Identify the blood parasite species.
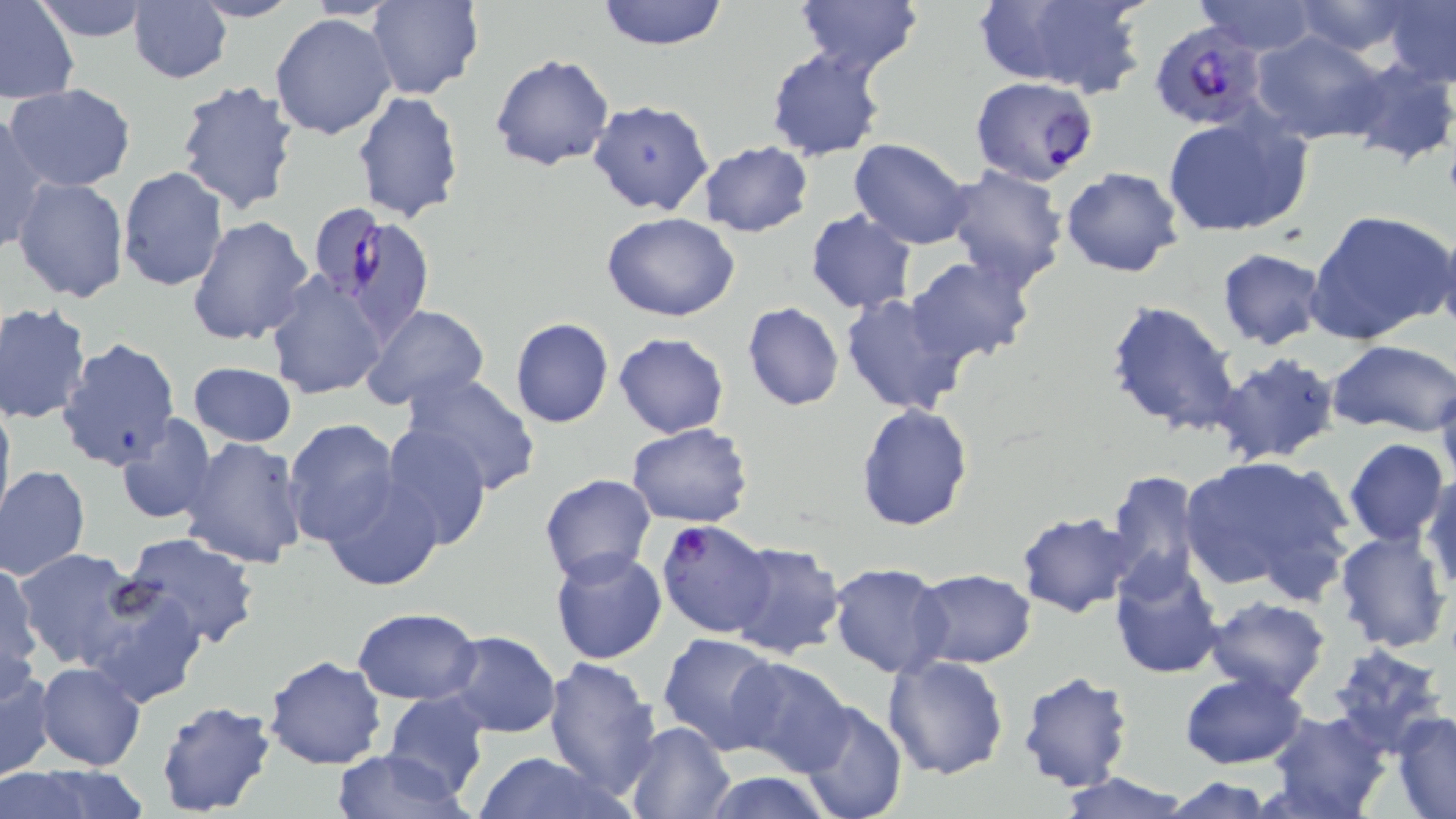

Plasmodium falciparum.

image size = 1456×819 pixels
uninfected red blood cell locations (subset) = approximate bounding boxes as (x1, y1, x2, y2) in pixels: (0, 0, 80, 104), (30, 0, 154, 42), (128, 0, 232, 85), (596, 0, 729, 50), (980, 0, 1147, 97), (1193, 0, 1322, 53), (189, 1, 302, 23), (366, 1, 483, 100), (795, 1, 923, 79), (1289, 1, 1419, 58), (1383, 1, 1455, 88), (269, 12, 399, 141), (1252, 31, 1389, 145), (766, 46, 889, 162), (489, 53, 615, 172), (1339, 57, 1456, 168), (175, 78, 302, 216), (5, 83, 137, 193), (352, 91, 465, 225), (587, 101, 715, 218), (1, 112, 51, 258), (1162, 112, 1312, 238), (847, 136, 976, 250), (698, 141, 813, 236), (941, 164, 1069, 292), (117, 166, 230, 293), (1060, 166, 1181, 278), (12, 176, 128, 304), (1307, 209, 1456, 346), (804, 210, 917, 314), (603, 212, 740, 323), (187, 215, 315, 345), (1435, 227, 1456, 336), (1216, 247, 1327, 349), (908, 256, 1033, 364), (264, 273, 388, 399), (839, 291, 968, 416), (1103, 299, 1241, 437), (0, 302, 94, 425), (742, 302, 844, 412), (361, 305, 491, 412), (509, 317, 614, 428), (612, 333, 730, 438), (61, 338, 179, 472), (1328, 340, 1456, 435), (1212, 351, 1341, 466), (187, 362, 298, 447), (401, 372, 543, 497), (1434, 379, 1456, 494), (0, 393, 15, 529), (855, 404, 972, 532), (113, 413, 218, 526), (283, 418, 402, 547), (625, 423, 753, 528), (377, 425, 491, 551), (1343, 437, 1450, 546), (180, 438, 310, 570), (1178, 455, 1353, 597), (0, 464, 91, 581), (1104, 469, 1205, 592), (321, 470, 442, 591), (1423, 471, 1456, 595), (539, 474, 657, 586), (1015, 510, 1137, 618), (1334, 527, 1452, 653), (119, 532, 262, 652), (725, 540, 847, 659), (13, 547, 147, 672), (550, 547, 669, 664), (1109, 555, 1225, 677), (0, 559, 41, 693), (828, 563, 951, 678), (908, 568, 1036, 669), (76, 579, 207, 709), (1203, 596, 1332, 702), (353, 607, 482, 705), (444, 631, 562, 737), (658, 634, 782, 754), (1326, 643, 1449, 754), (263, 656, 385, 771), (544, 656, 663, 801), (882, 656, 1010, 780), (726, 658, 853, 776), (35, 662, 146, 772), (0, 664, 56, 780), (1016, 669, 1136, 791), (1178, 672, 1308, 769), (383, 690, 490, 799), (153, 699, 276, 817), (794, 699, 907, 819), (1267, 710, 1392, 819), (1391, 711, 1456, 817), (624, 721, 733, 819), (332, 749, 470, 818), (472, 751, 626, 819), (24, 764, 149, 819), (2, 769, 85, 818), (1052, 771, 1193, 818), (696, 772, 840, 818), (1154, 776, 1284, 817)
stain = May-Grünwald-Giemsa
preparation = thin blood smear
field of view = single
modality = optical microscopy
Plasmodium falciparum-infected red blood cell locations (subset) = approximate bounding boxes as (x1, y1, x2, y2) in pixels: (1149, 21, 1266, 129), (310, 203, 388, 303), (655, 519, 777, 637)
magnification = 1000x